Describe the morphology of the red blood cells.
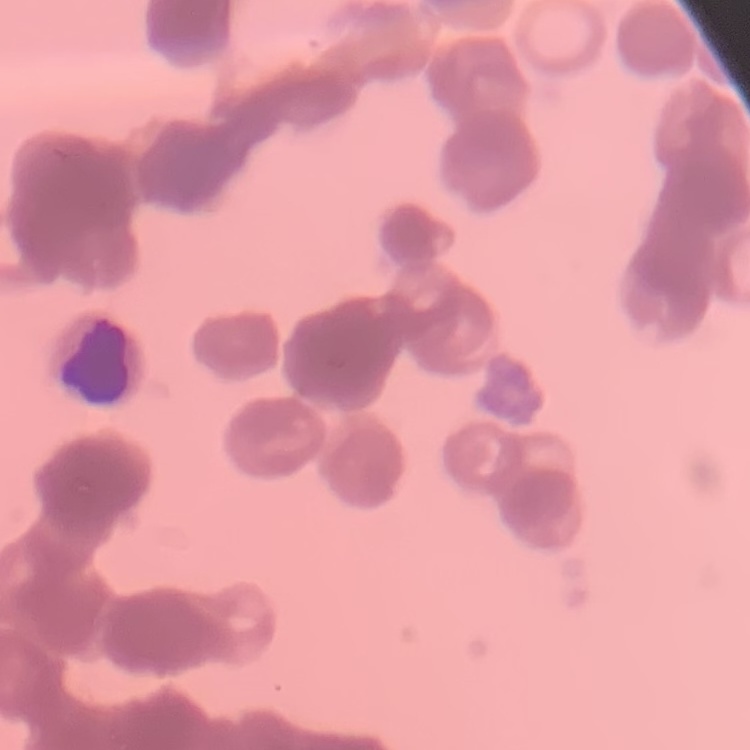

They show rouleaux formation.

image_type: square crop of a larger photomicrograph
preparation: thin peripheral smear
stain: Field's or Giemsa